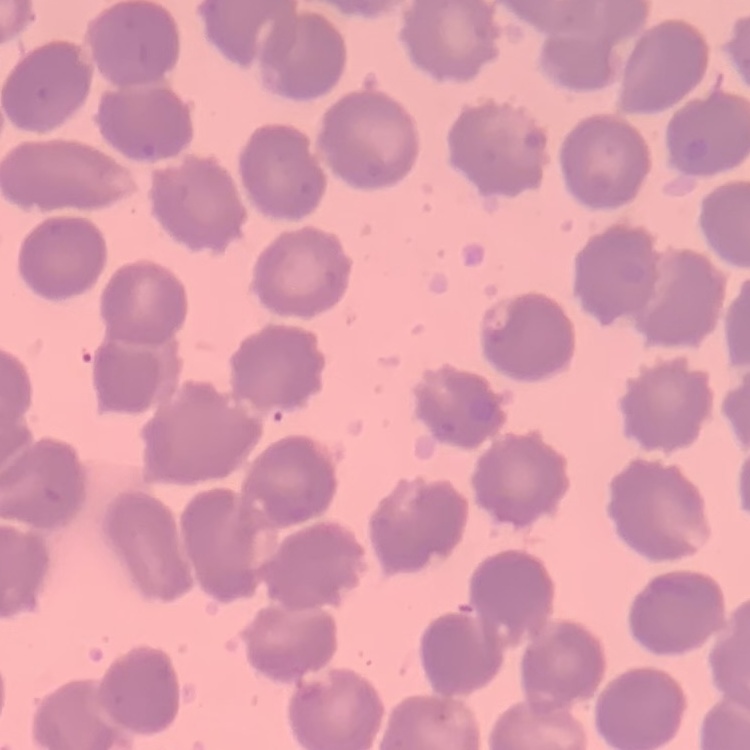

Summary:
  - Erythrocyte morphology: no rouleaux formation
  - Stain: Field's or Giemsa
  - Preparation: thin peripheral smear
  - Image type: square crop of a larger photomicrograph